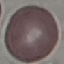

Result: negative for malaria parasites. Thin blood film. Acquired by smartphone through the microscope eyepiece. Cell patch, automatically extracted from a larger field of view and resized to 64 × 64 pixels. Giemsa stain.